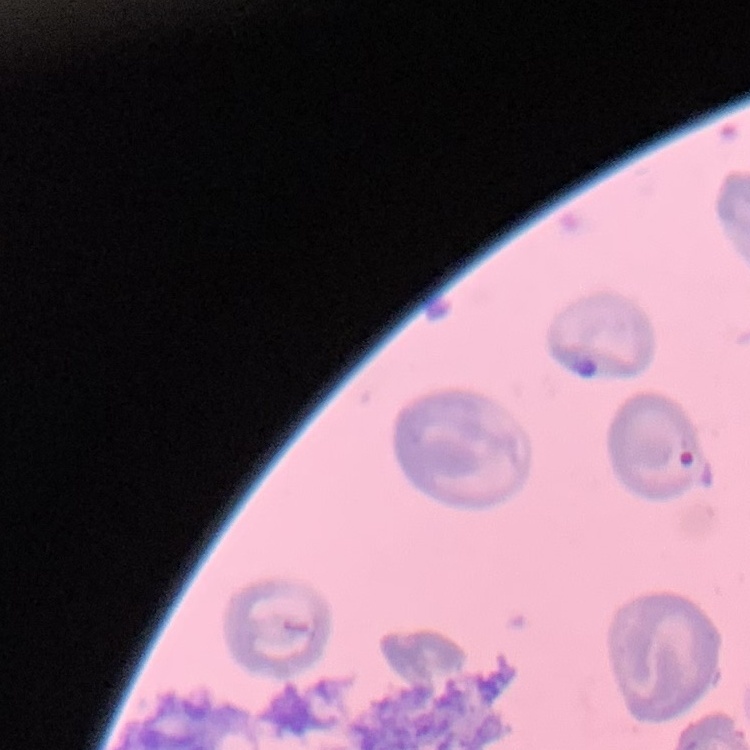

red blood cell morphology = no rouleaux formation
stain = Field's or Giemsa
preparation = thin peripheral smear
image type = square crop of a larger photomicrograph